Give the location of every parasitized red blood cell.
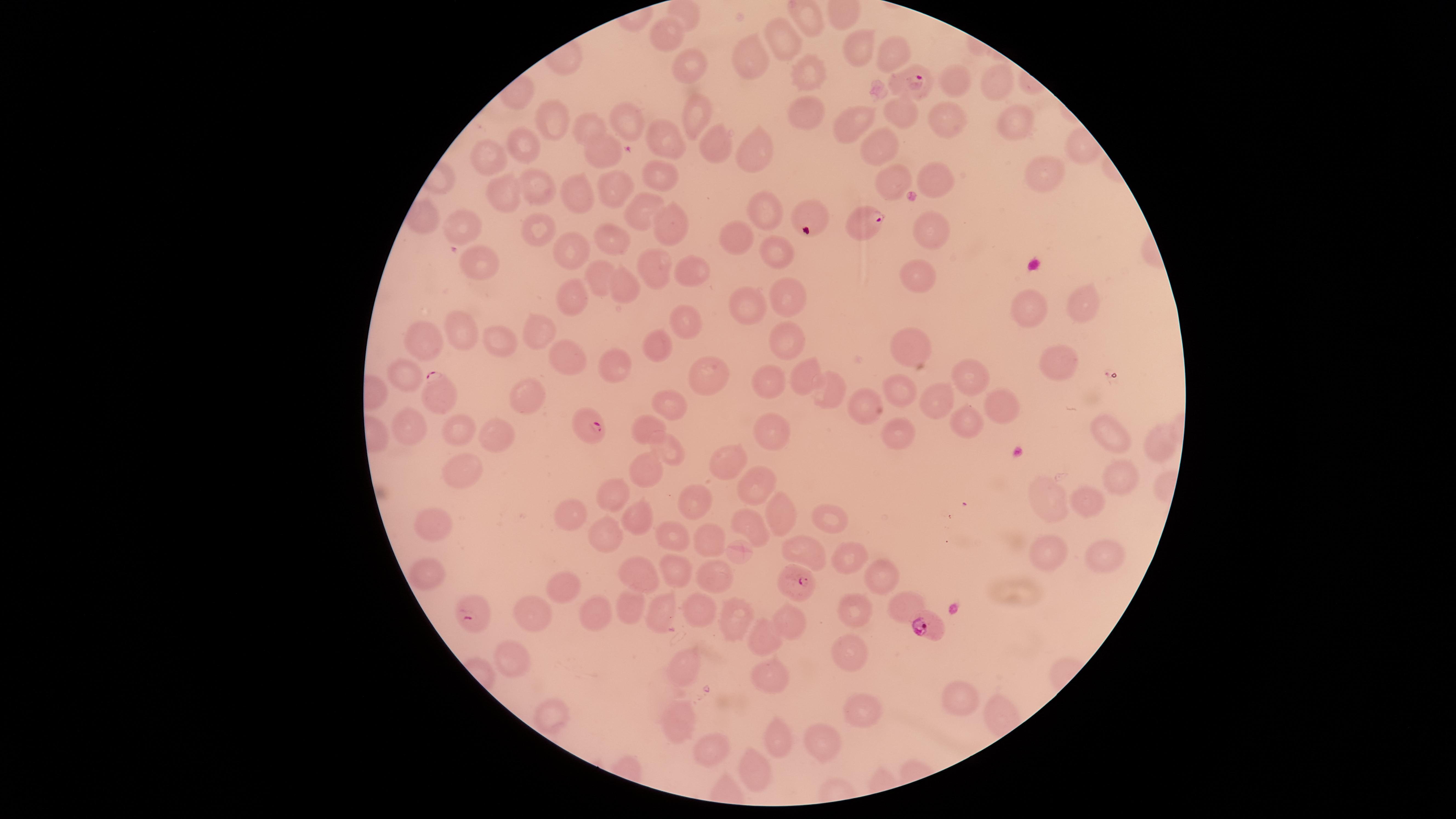

Approximate marker points as [x, y] in pixels.
Parasitized red blood cells: [913, 80], [861, 222], [435, 392], [591, 425], [799, 585], [474, 608], [927, 624].

preparation = thin blood smear
capture = smartphone photograph through the microscope eyepiece
species = Plasmodium falciparum
visible region = circular
uninfected red blood cells = approximate marker points as [x, y] in pixels: [784, 34], [668, 38], [855, 48], [888, 50], [752, 60], [691, 63], [811, 76], [954, 80], [996, 83], [809, 114], [696, 115], [900, 115], [550, 119], [947, 119], [627, 121], [849, 123], [1014, 124], [585, 131], [668, 139], [718, 142], [885, 147], [525, 149], [757, 149], [605, 152], [497, 157], [1044, 176], [657, 178], [937, 181], [893, 183], [540, 187], [614, 191], [577, 194], [507, 198], [641, 207], [763, 210], [807, 211], [670, 221], [461, 222], [539, 226], [935, 228], [613, 236], [733, 238], [573, 246], [779, 256], [653, 266], [480, 267], [689, 272], [921, 274], [597, 275], [624, 286], [576, 293], [785, 301], [1078, 302], [749, 305], [1029, 310], [685, 324], [462, 328], [543, 329], [430, 340], [787, 340], [911, 343], [504, 344], [655, 344], [573, 356], [1056, 361], [619, 364], [705, 373], [808, 373], [971, 374], [409, 375], [771, 379], [900, 386], [830, 392], [530, 397], [937, 398], [864, 402], [675, 405], [999, 409], [969, 423], [408, 425], [459, 425], [771, 428], [650, 429], [900, 431], [1108, 435], [494, 440], [1152, 447], [672, 449], [734, 462], [639, 473], [461, 477], [1121, 478], [754, 483], [1057, 496], [1090, 499], [695, 502], [613, 504], [779, 516], [832, 516], [636, 517], [571, 519], [434, 524], [751, 524], [674, 532], [602, 534], [708, 538], [807, 551], [1045, 555], [1106, 557], [846, 561], [432, 570], [677, 570], [632, 573], [878, 576], [716, 578], [561, 581], [629, 602], [902, 608], [700, 609], [662, 611], [856, 612], [532, 614], [737, 615], [593, 618], [792, 620], [767, 639], [854, 657], [686, 662], [512, 663], [767, 679], [966, 694], [552, 712], [857, 720], [678, 721], [779, 738], [710, 748], [813, 748], [754, 770]
image size = 1456×819 pixels
stain = Giemsa
field of view = single